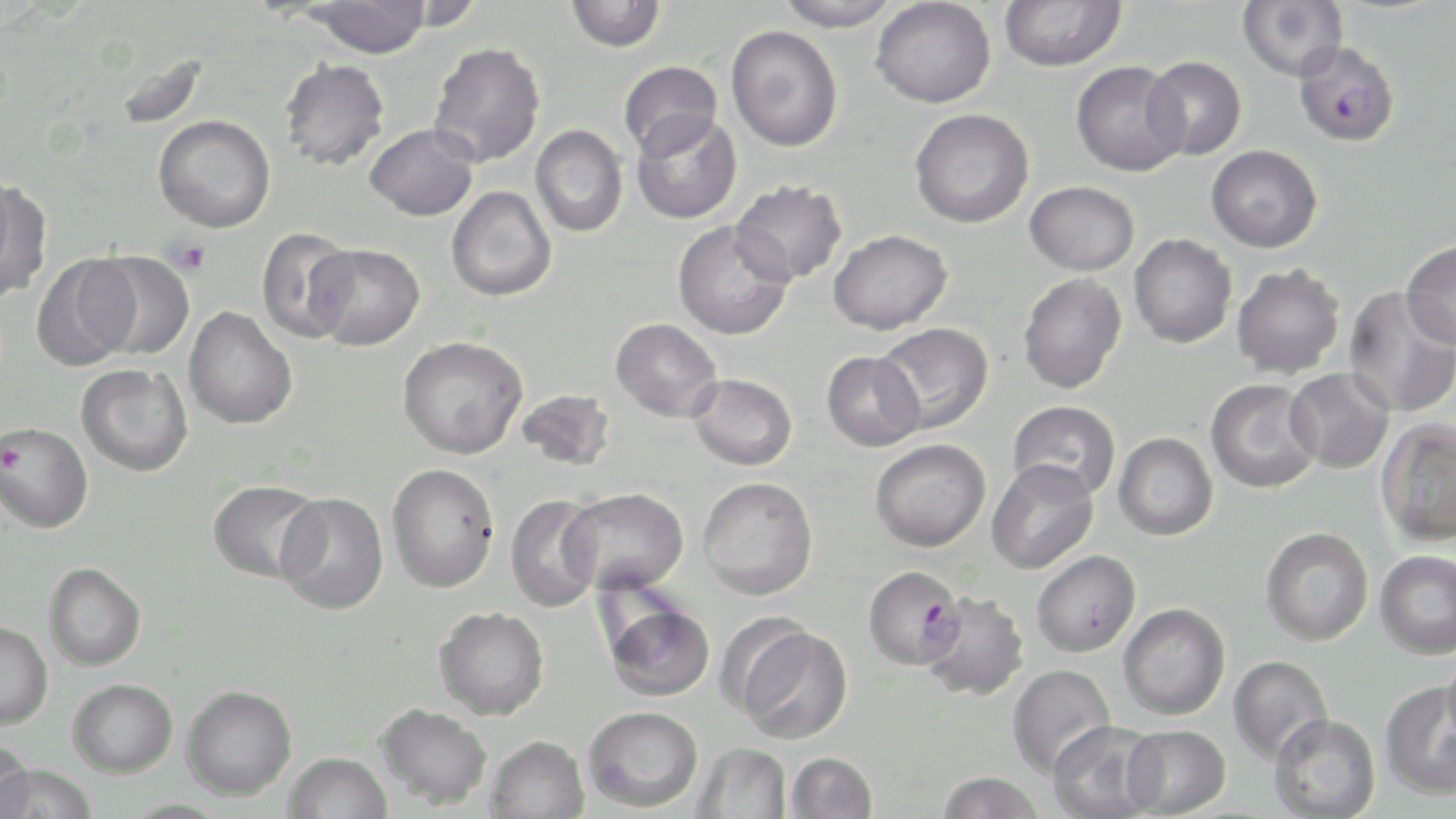
Approximate bounding boxes as [x1, y1, x2, y2] in pixels. Plasmodium falciparum-infected red blood cell locations: [1293, 41, 1401, 147], [862, 564, 965, 670]. Platelet locations: [166, 238, 212, 276]. Uninfected red blood cell locations: [305, 0, 431, 58], [565, 0, 666, 52], [774, 0, 902, 32], [871, 0, 996, 108], [999, 0, 1126, 72], [1237, 0, 1348, 81], [726, 26, 843, 152], [428, 43, 546, 168], [1143, 56, 1247, 160], [280, 59, 389, 171], [618, 61, 723, 157], [1070, 61, 1188, 177], [909, 108, 1034, 228], [631, 111, 742, 224], [153, 114, 276, 233], [365, 124, 478, 221], [530, 125, 628, 238], [1206, 145, 1322, 252], [0, 179, 50, 303], [730, 180, 847, 286], [1025, 181, 1139, 275], [446, 186, 556, 301], [673, 220, 794, 340], [256, 227, 359, 343], [828, 229, 952, 335], [1129, 233, 1237, 348], [1400, 239, 1456, 350], [309, 243, 425, 351], [86, 251, 195, 360], [31, 253, 140, 371], [1231, 263, 1345, 378], [1018, 272, 1127, 394], [1343, 286, 1456, 418], [183, 307, 297, 429], [610, 318, 723, 422], [873, 322, 994, 433], [397, 336, 527, 459], [821, 351, 925, 451], [76, 363, 192, 476], [1284, 367, 1395, 473], [688, 373, 797, 470], [1205, 379, 1321, 494], [516, 388, 616, 472], [1007, 400, 1120, 502], [1374, 418, 1456, 547], [0, 422, 93, 532], [1113, 432, 1218, 541], [870, 438, 991, 552], [986, 459, 1098, 574], [386, 463, 499, 592], [698, 476, 818, 600], [208, 480, 323, 583], [561, 488, 688, 595], [275, 492, 388, 615], [505, 494, 603, 612], [1261, 527, 1373, 646], [1375, 549, 1456, 660], [1031, 550, 1141, 657], [44, 562, 146, 671], [918, 590, 1029, 701], [603, 597, 716, 702], [1118, 603, 1230, 720], [434, 606, 549, 719], [0, 621, 52, 730], [735, 625, 853, 743], [1443, 649, 1456, 748], [1228, 655, 1332, 764], [1006, 664, 1115, 778], [68, 678, 178, 777], [1379, 680, 1456, 801], [182, 684, 297, 800], [375, 703, 492, 810], [582, 706, 703, 811], [1268, 713, 1381, 819], [1047, 721, 1163, 818], [1121, 725, 1231, 817], [484, 735, 590, 819], [0, 740, 34, 819], [693, 742, 792, 818], [786, 751, 878, 818], [284, 752, 392, 819], [0, 763, 100, 819], [935, 771, 1046, 819], [119, 798, 234, 818]. Slide-level diagnosis: Plasmodium falciparum. One field of a larger specimen. Captured at 1000x magnification. Light microscopy. May-Grünwald-Giemsa stain. Thin blood film. Image is 1456×819 pixels.